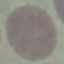

Result: negative for malaria parasites. Photographed with a smartphone camera at the microscope eyepiece. Thin smear of blood. Giemsa-stained preparation. Automatically extracted cell patch, resized to 64 × 64 pixels.